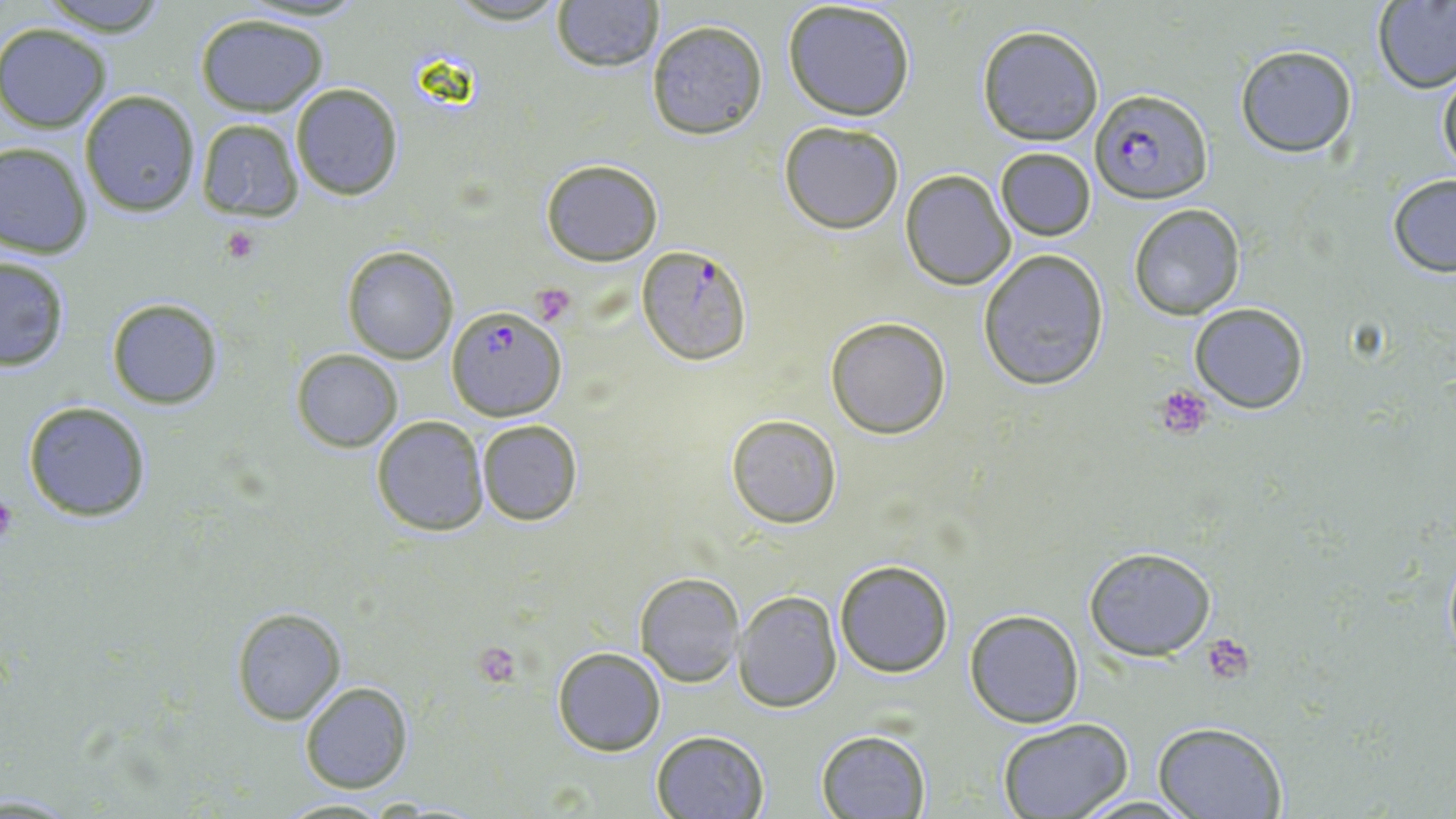
Summary:
  - Coordinate format: approximate bounding boxes as (x1,y1)-(x2,y2) corner pairs in pixels
  - Platelet locations: (222,229)-(261,263), (536,289)-(578,320), (1155,385)-(1215,439), (0,489)-(17,547), (1203,633)-(1253,681), (474,644)-(522,685)
  - Plasmodium falciparum-infected red blood cell locations: (1091,88)-(1210,204), (638,245)-(752,364), (446,306)-(567,420)
  - Uninfected red blood cell locations: (36,0)-(170,35), (443,0)-(572,27), (782,0)-(917,121), (552,1)-(664,73), (1372,1)-(1456,95), (194,13)-(330,116), (646,20)-(768,139), (976,24)-(1104,146), (0,25)-(111,132), (1234,45)-(1358,159), (1436,62)-(1456,183), (290,83)-(406,200), (79,91)-(199,216), (194,117)-(304,222), (779,121)-(904,233), (0,142)-(95,259), (994,146)-(1096,242), (540,159)-(664,266), (899,168)-(1015,291), (1386,174)-(1456,276), (1127,204)-(1246,320), (342,244)-(458,364), (978,248)-(1109,389), (0,254)-(72,373), (106,297)-(224,410), (1189,302)-(1309,414), (825,316)-(953,439), (292,349)-(402,452), (22,400)-(153,522), (370,415)-(489,537), (726,415)-(843,529), (475,420)-(584,526), (1083,547)-(1216,660), (833,560)-(955,677), (634,571)-(743,687), (735,590)-(843,712), (230,606)-(346,725), (964,609)-(1085,729), (552,646)-(667,756), (300,681)-(414,795), (997,719)-(1136,818), (1153,721)-(1289,819), (813,728)-(932,818), (652,729)-(769,818), (1073,793)-(1200,817), (276,796)-(397,818)
  - Slide-level diagnosis: Plasmodium falciparum
  - Image size: 1456×819 pixels
  - Preparation: thin blood smear
  - Magnification: 1000x
  - Modality: light microscopy
  - Field of view: single
  - Stain: May-Grünwald-Giemsa